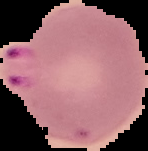

Summary:
  - Preparation: thin blood smear
  - Image size: 148×151 pixels
  - Image type: segmented cell region with the area outside set to black
  - Result: malaria parasites detected